State which parasite is depicted.
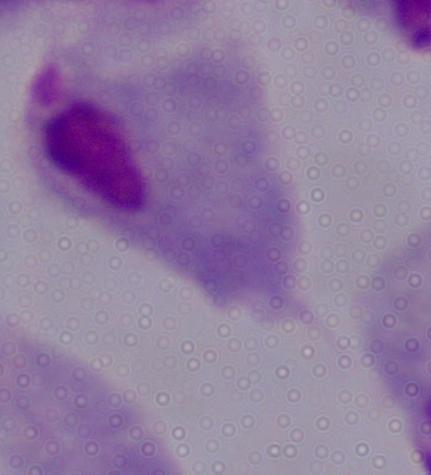
This is a trichomonad.

Summary:
  - Magnification: 1000x
  - Modality: micrograph